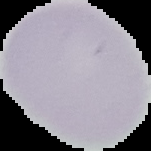

The area outside the segmented cell region is set to black. Image is 151×151 pixels. From a thin blood smear. Malaria status: uninfected.